Report the malaria status of this cell.
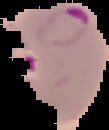

It is parasitized.

Image is 109×130 pixels. From a thin blood film. Cell region segmented out of the field of view; the surrounding area is masked to black.